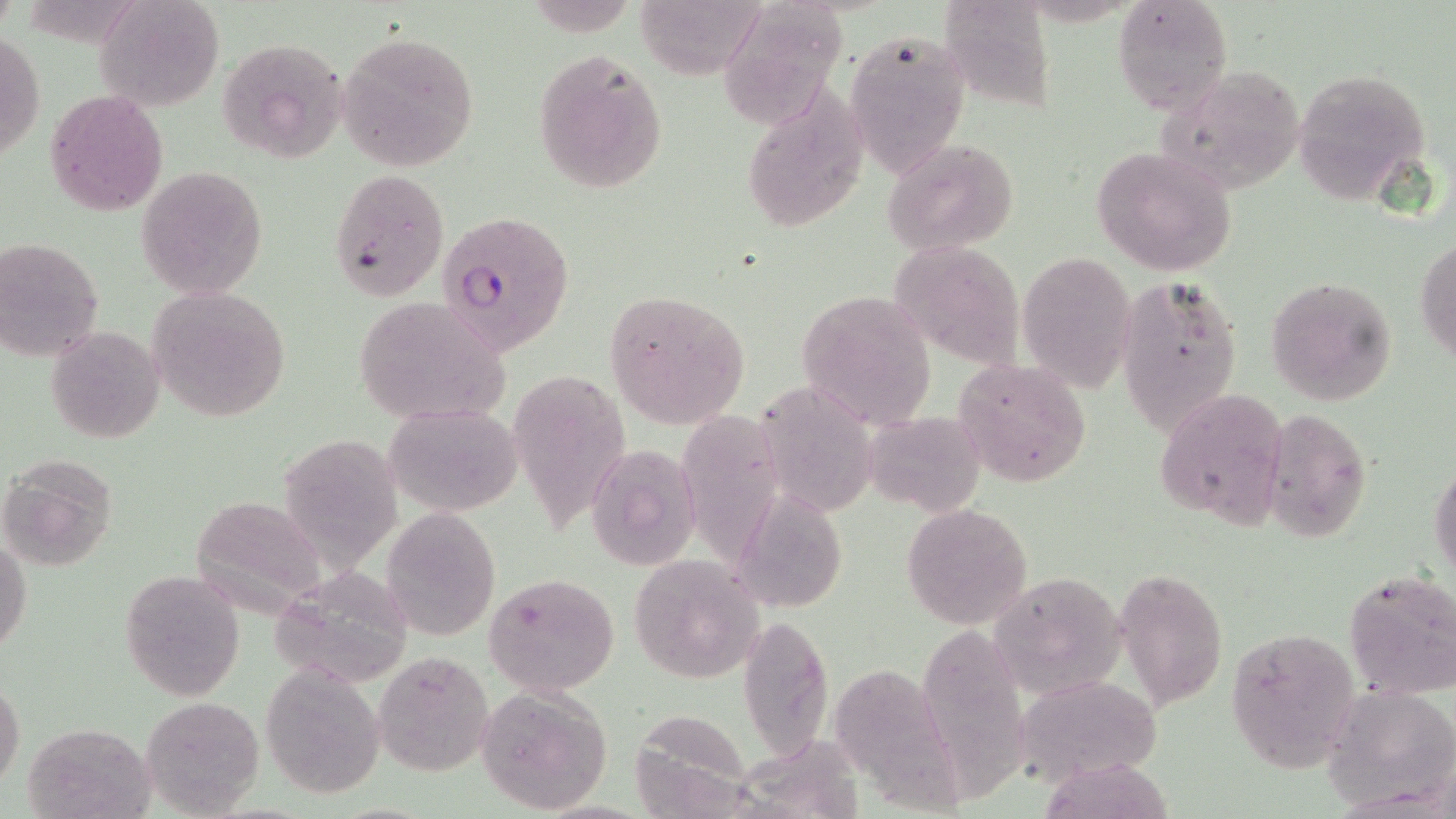

Summary:
  - Coordinate format: approximate bounding boxes as (x1, y1, x2, y2) in pixels
  - Uninfected red blood cell locations: (96, 0, 224, 112), (938, 0, 1057, 114), (1111, 0, 1234, 114), (631, 2, 755, 79), (719, 4, 853, 139), (1, 28, 43, 166), (337, 29, 480, 173), (843, 29, 971, 179), (214, 36, 347, 164), (532, 47, 668, 193), (1157, 63, 1306, 195), (1291, 65, 1434, 201), (44, 88, 169, 217), (741, 88, 871, 231), (883, 137, 1021, 257), (1090, 145, 1240, 275), (136, 165, 268, 299), (327, 169, 450, 301), (1416, 236, 1456, 364), (0, 239, 104, 362), (897, 251, 1035, 374), (1017, 251, 1138, 396), (1117, 275, 1242, 431), (1266, 275, 1397, 406), (145, 285, 294, 422), (603, 288, 753, 429), (794, 290, 937, 430), (349, 295, 511, 426), (45, 325, 165, 443), (953, 355, 1095, 487), (517, 374, 638, 543), (760, 379, 877, 523), (1157, 388, 1289, 527), (386, 402, 522, 516), (668, 406, 783, 578), (1261, 406, 1373, 546), (858, 413, 992, 519), (283, 436, 405, 587), (585, 442, 701, 570), (1, 456, 118, 571), (1429, 462, 1456, 585), (197, 497, 322, 625), (736, 497, 854, 610), (902, 502, 1033, 631), (380, 505, 501, 641), (0, 536, 31, 657), (627, 553, 768, 683), (272, 560, 425, 678), (119, 569, 245, 702), (990, 570, 1129, 699), (1115, 570, 1228, 708), (1344, 570, 1456, 703), (485, 572, 620, 696), (739, 614, 834, 761), (926, 626, 1036, 802), (1226, 629, 1361, 772), (372, 651, 493, 775), (835, 652, 965, 816), (260, 666, 384, 798), (0, 676, 24, 795), (1007, 678, 1180, 791), (1322, 681, 1456, 809), (473, 684, 613, 814), (141, 696, 267, 817), (647, 709, 761, 819), (21, 721, 157, 819), (741, 739, 865, 819), (1047, 755, 1177, 819)
  - Plasmodium falciparum-infected red blood cell locations: (434, 208, 574, 357)
  - Slide-level diagnosis: Plasmodium falciparum
  - Preparation: thin blood film
  - Image size: 1456×819 pixels
  - Field of view: one of a larger specimen
  - Stain: May-Grünwald-Giemsa
  - Modality: optical microscopy
  - Magnification: 1000x